Classify this cell by malaria status.
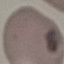
It is uninfected.

{
  "stain": "Giemsa",
  "preparation": "thin smear",
  "capture": "smartphone through the microscope eyepiece",
  "image_type": "automatically extracted cell patch, resized to 64 × 64 pixels"
}